Describe the morphology of the erythrocytes.
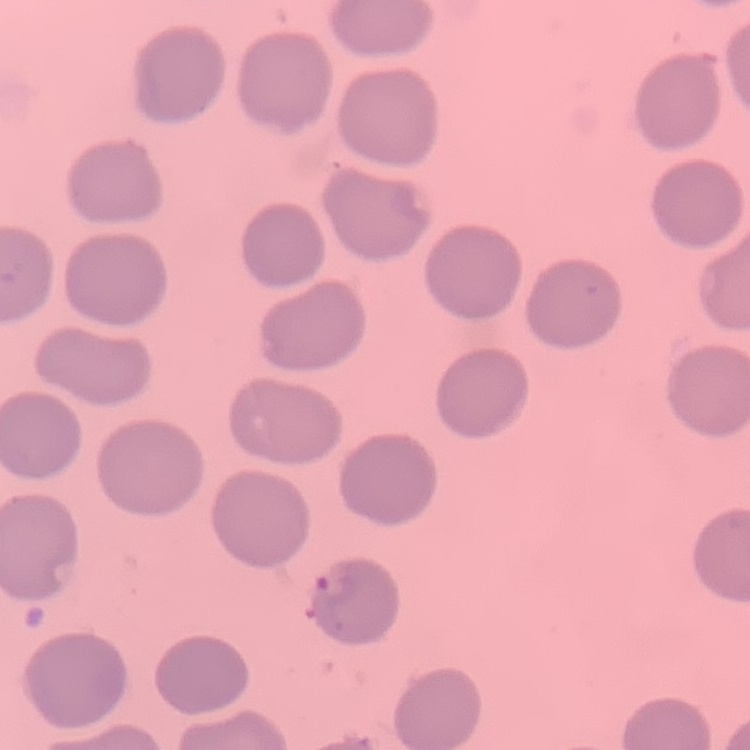
No rouleaux formation.

One tile cut from a larger photomicrograph. Stained with either Field's or Giemsa. Thin peripheral smear.